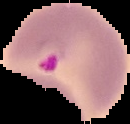 Image is 130×124 pixels. Malaria status: parasitized. From a thin blood film. The area outside the segmented cell region is set to black.